Give the preparation type.
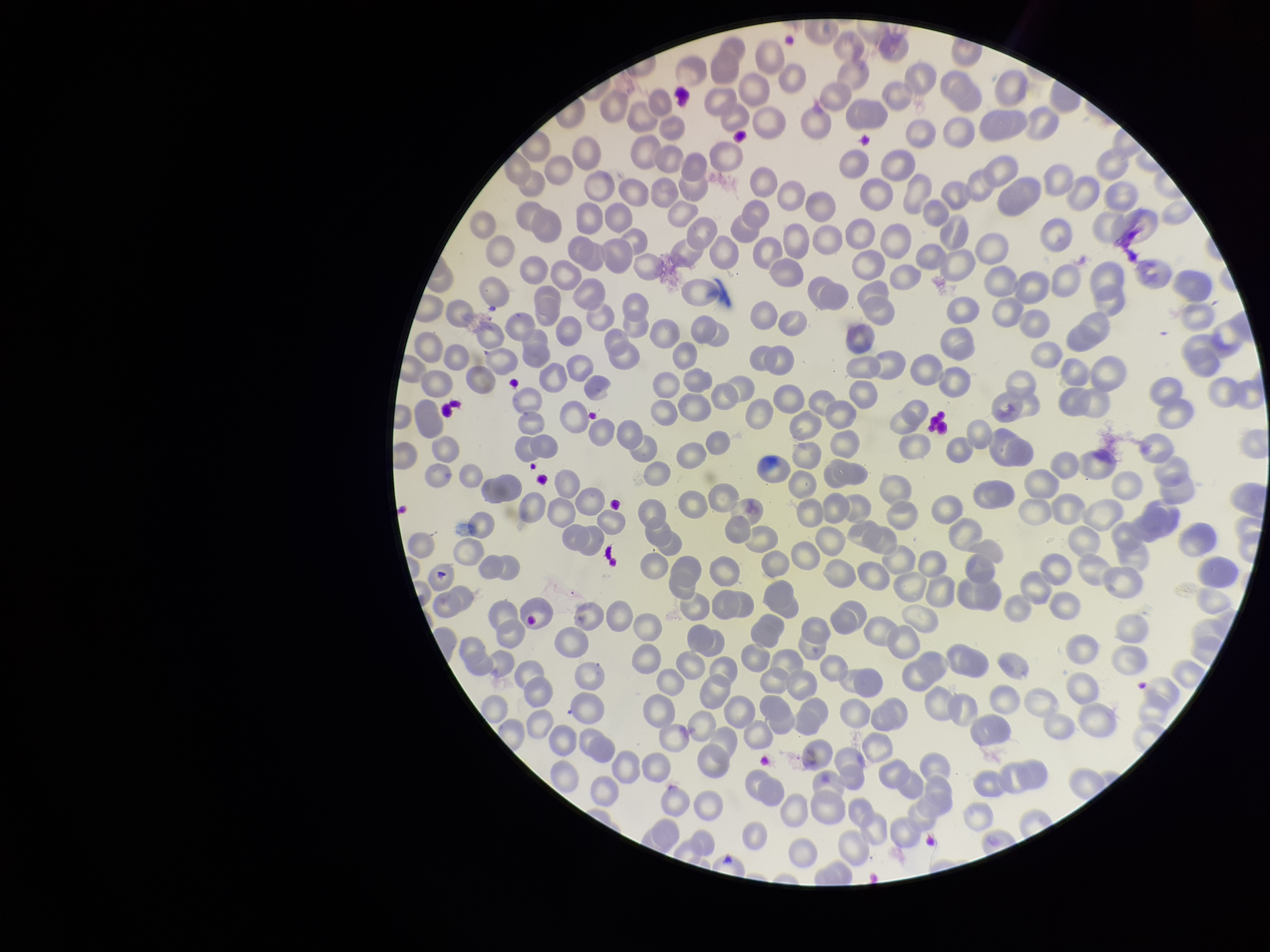

A thin smear.

red blood cell count = 284
stain = Giemsa
field of view = single
species reported for this patient = Plasmodium falciparum
parasitized red blood cells = none seen
image size = 1270×952 pixels
parasitized red blood cell count = 0
patient malaria status = infected
capture = smartphone photograph through the microscope eyepiece